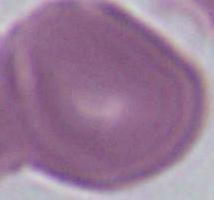 Captured at 1000x magnification. A red blood cell is shown. Photomicrograph.